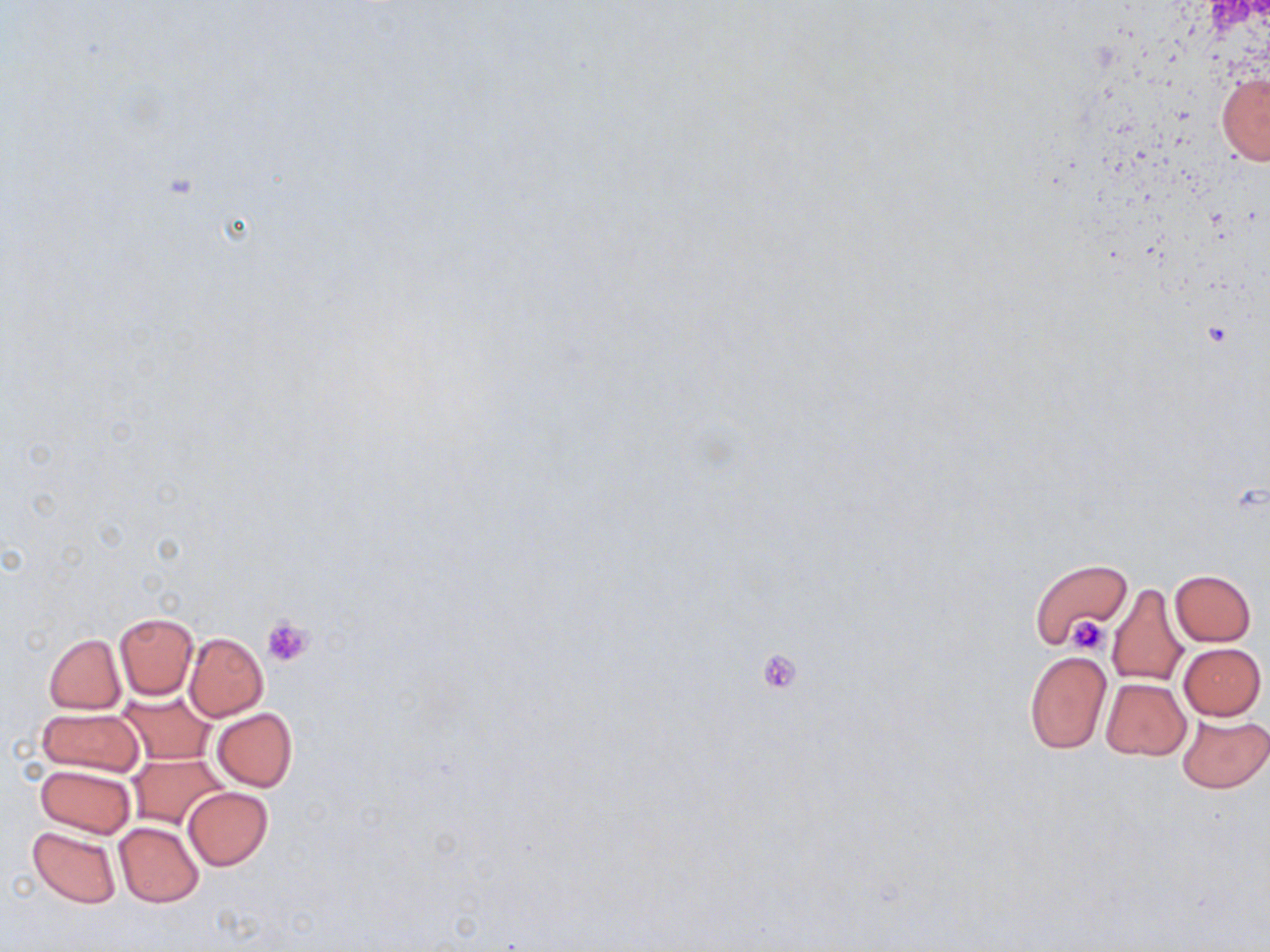

Summary:
  - Coordinate format: approximate bounding boxes as [x1, y1, x2, y2] in pixels
  - Uninfected red blood cell locations: [1216, 69, 1270, 165], [1029, 559, 1131, 648], [1170, 569, 1256, 646], [1107, 582, 1189, 689], [114, 612, 198, 699], [184, 632, 268, 721], [44, 633, 125, 714], [1179, 642, 1266, 719], [1025, 651, 1110, 753], [1101, 678, 1191, 760], [117, 691, 217, 765], [36, 708, 143, 778], [212, 709, 297, 791], [1176, 712, 1270, 794], [127, 753, 227, 830], [35, 763, 136, 838], [183, 787, 272, 870], [114, 821, 205, 907], [28, 825, 122, 908]
  - Platelet locations: [262, 616, 314, 668], [1069, 616, 1110, 654], [756, 648, 804, 694]
  - Slide-level diagnosis: negative for blood parasites
  - Stain: May-Grünwald-Giemsa
  - Magnification: 1000x
  - Modality: light microscopy
  - Field of view: single
  - Preparation: thin blood smear
  - Image size: 1270×952 pixels